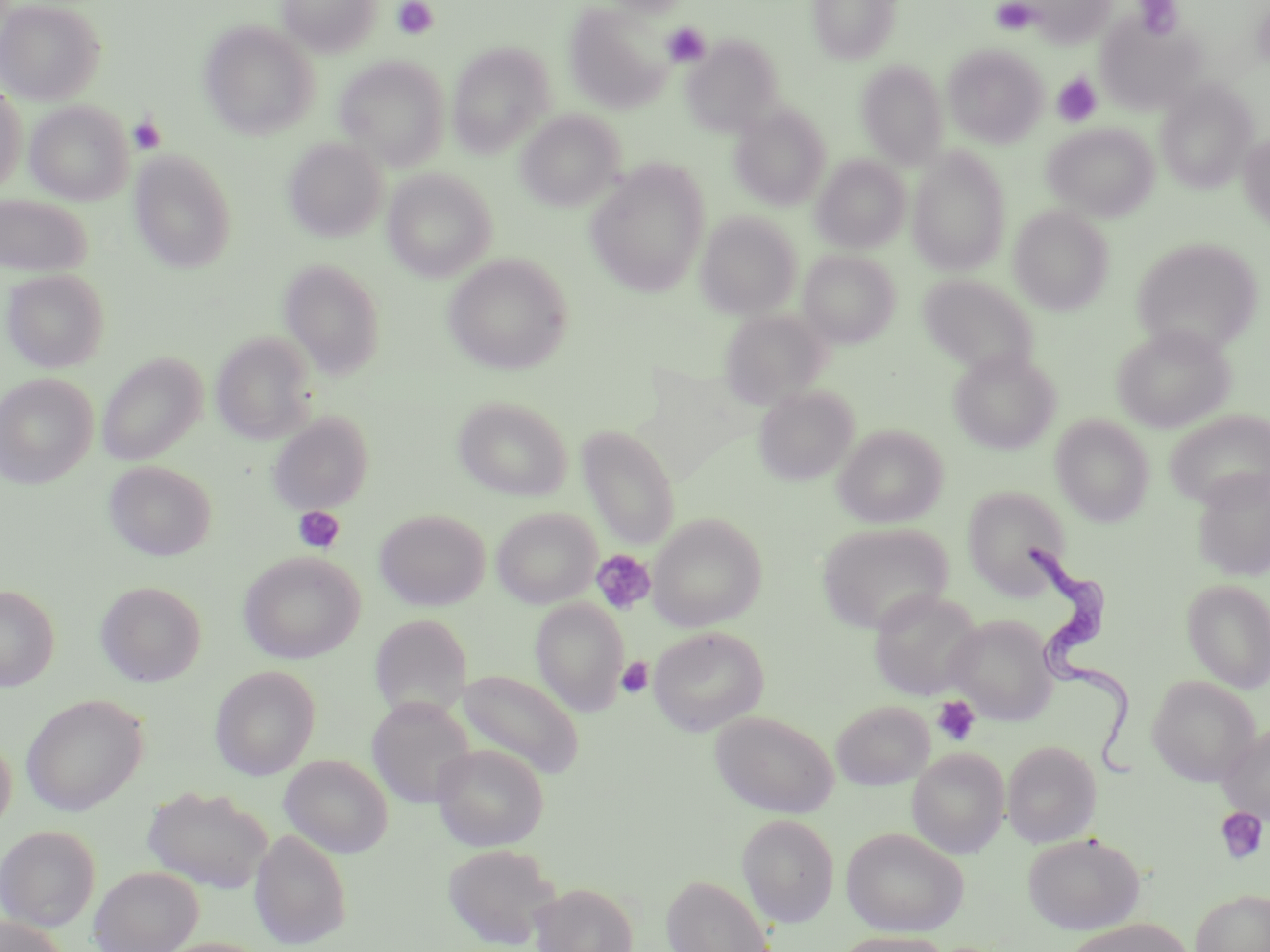

{
  "slide_level_diagnosis": "Trypanosoma brucei",
  "platelet_locations": "approximate bounding boxes as (x1,y1)-(x2,y2) corner pairs in pixels: (392,0)-(439,40), (1135,0)-(1182,40), (991,1)-(1037,34), (661,22)-(711,67), (1052,73)-(1102,127), (128,114)-(166,155), (293,507)-(345,553), (592,549)-(656,614), (617,657)-(654,698), (932,695)-(981,746), (1214,807)-(1268,864)",
  "uninfected_red_blood_cell_locations": "approximate bounding boxes as (x1,y1)-(x2,y2) corner pairs in pixels: (0,0)-(106,105), (278,0)-(382,56), (600,0)-(693,17), (806,0)-(903,65), (1019,0)-(1116,48), (564,3)-(674,113), (1096,11)-(1208,115), (199,21)-(319,139), (682,34)-(784,136), (447,42)-(556,156), (942,43)-(1048,147), (334,56)-(449,169), (857,61)-(949,168), (1155,80)-(1258,193), (0,84)-(26,195), (26,101)-(133,205), (729,103)-(831,210), (517,110)-(624,211), (1043,122)-(1159,221), (1238,130)-(1270,231), (283,137)-(388,242), (907,146)-(1012,275), (130,150)-(237,273), (812,154)-(911,253), (585,161)-(710,296), (383,169)-(497,282), (0,194)-(91,277), (1009,206)-(1114,315), (696,212)-(801,319), (1130,236)-(1264,355), (799,250)-(900,347), (443,253)-(573,375), (279,259)-(386,378), (2,268)-(110,372), (919,275)-(1038,377), (719,309)-(831,408), (1112,324)-(1236,432), (211,332)-(317,444), (948,349)-(1061,455), (97,353)-(207,466), (0,373)-(97,489), (754,385)-(858,485), (453,396)-(573,500), (1167,409)-(1269,508), (268,412)-(373,515), (1050,415)-(1155,526), (577,424)-(681,548), (835,424)-(947,528), (104,460)-(217,561), (1191,468)-(1270,581), (962,485)-(1072,598), (491,507)-(601,608), (374,508)-(490,610), (647,513)-(766,631), (816,521)-(953,634), (238,551)-(365,664), (1182,578)-(1270,692), (95,580)-(206,687), (0,584)-(59,691), (868,589)-(984,700), (531,598)-(629,716), (945,613)-(1058,724), (648,626)-(769,735), (210,665)-(321,780), (455,668)-(585,779), (1148,676)-(1259,786), (20,694)-(149,816), (367,698)-(476,808), (832,700)-(935,789), (710,711)-(839,818), (1218,721)-(1270,824), (0,733)-(16,833), (1002,740)-(1102,847), (431,743)-(549,850), (907,747)-(1010,858), (279,754)-(393,858), (142,785)-(273,894), (737,813)-(839,926), (0,824)-(101,931), (841,826)-(969,936), (250,829)-(351,949), (1022,832)-(1144,934), (442,843)-(560,949), (89,865)-(203,952), (661,874)-(775,952), (530,882)-(639,952), (1191,888)-(1270,952), (0,916)-(69,952), (1063,918)-(1196,952), (831,931)-(952,952), (153,936)-(270,952)",
  "image_size": "1270×952 pixels",
  "trypanosoma_brucei_locations": "approximate bounding boxes as (x1,y1)-(x2,y2) corner pairs in pixels: (1019,534)-(1148,797)",
  "magnification": "1000x",
  "stain": "May-Grünwald-Giemsa",
  "preparation": "thin blood smear",
  "field_of_view": "one of a larger specimen",
  "modality": "light microscopy"
}